Classify this cell by malaria status.
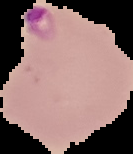
It is parasitized.

The area outside the segmented cell region is set to black. From a thin blood smear. Image is 133×154 pixels.